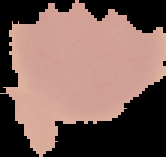

preparation: thin blood film
image_type: cell region segmented out of the field of view; surrounding area masked to black
image_size: 166×157 pixels
malaria_status: uninfected